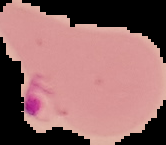
Summary:
  - Preparation: thin blood smear
  - Result: malaria parasites identified
  - Image size: 166×145 pixels
  - Image type: segmented cell region on a black background